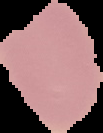
image size = 103×133 pixels
preparation = thin blood smear
image type = segmented cell region with the area outside set to black
result = negative for Plasmodium parasites